State which cell type is depicted.
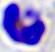

This is a leukocyte.

Summary:
  - Modality: photomicrograph
  - Magnification: 400x